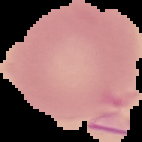

Result: negative for malaria parasites. The area outside the segmented cell region is set to black. Image is 142×142 pixels. From a thin blood smear.